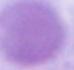

identification = erythrocyte
magnification = 1000x
modality = photomicrograph